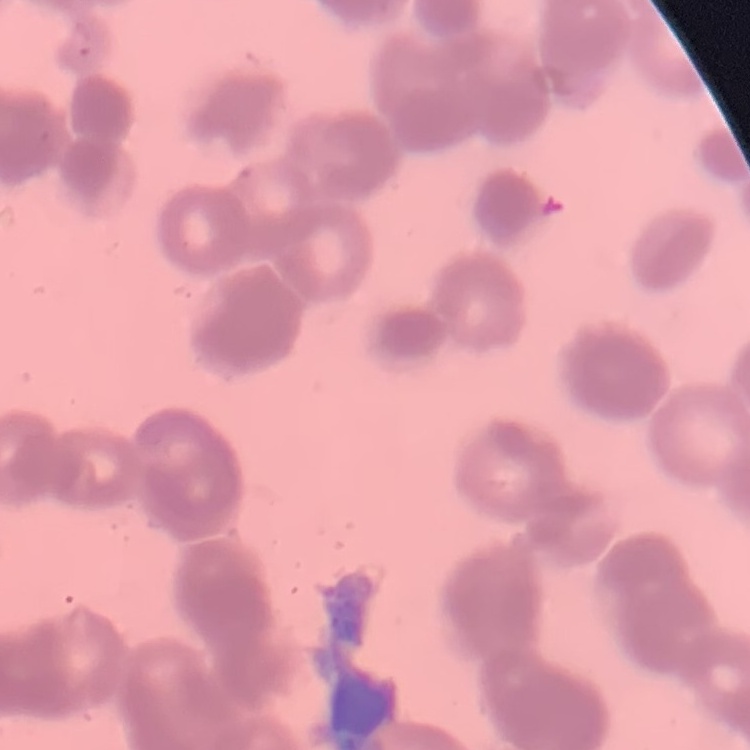 The erythrocytes show rouleaux formation. Stained with either Field's or Giemsa. Thin blood smear. Square crop of a larger photomicrograph.